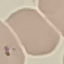 Malaria status: parasitized. Photographed with a smartphone camera at the microscope eyepiece. Cell patch, automatically extracted from a larger field of view and resized to 64 × 64 pixels. Thin blood smear. Giemsa stain.